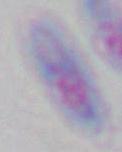

Summary:
  - Identification: Toxoplasma gondii
  - Magnification: 1000x
  - Modality: micrograph